Classify this cell by malaria status.
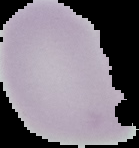

Uninfected.

Image is 139×148 pixels. The area outside the segmented cell region is set to black. From a thin blood film.